Assess the morphology of the erythrocytes.
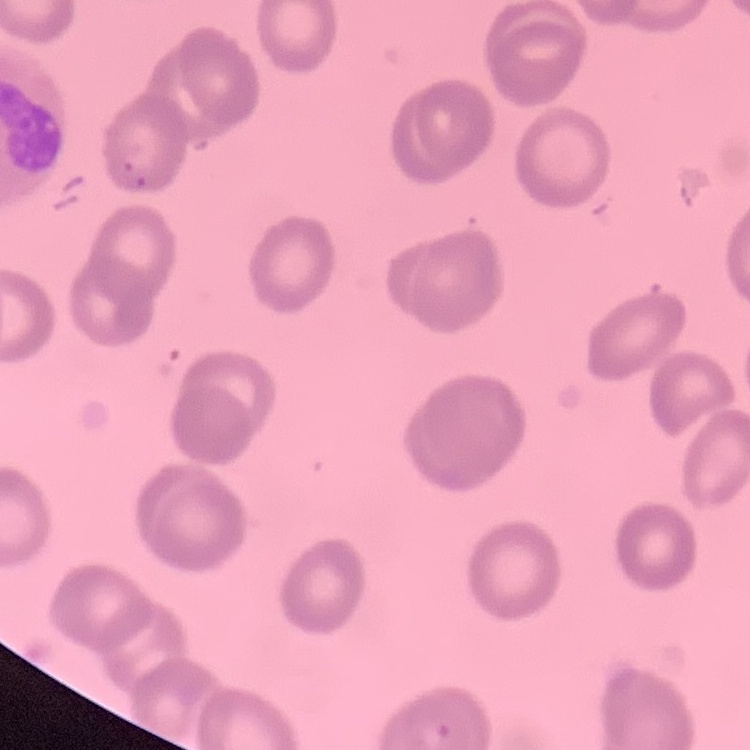

No rouleaux formation.

Square crop of a larger photomicrograph. Stained with either Field's or Giemsa. Thin peripheral smear.